Comment on the morphology of the erythrocytes.
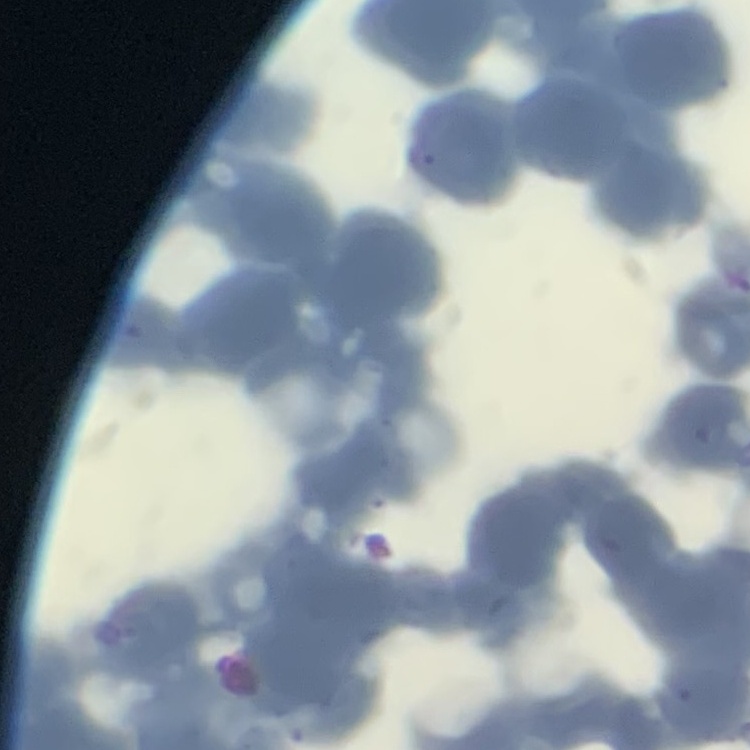

They show rouleaux formation.

image_type: square crop of a larger photomicrograph
stain: Field's or Giemsa
preparation: thin blood film